Assess this cell for malaria.
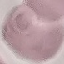

Uninfected.

Automatically extracted cell patch, resized to 64 × 64 pixels. Thin blood smear. Giemsa stain. Acquired by smartphone through the microscope eyepiece.